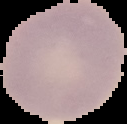

Summary:
  - Preparation: thin blood smear
  - Image size: 127×124 pixels
  - Image type: segmented cell region on a black background
  - Result: no Plasmodium parasites detected